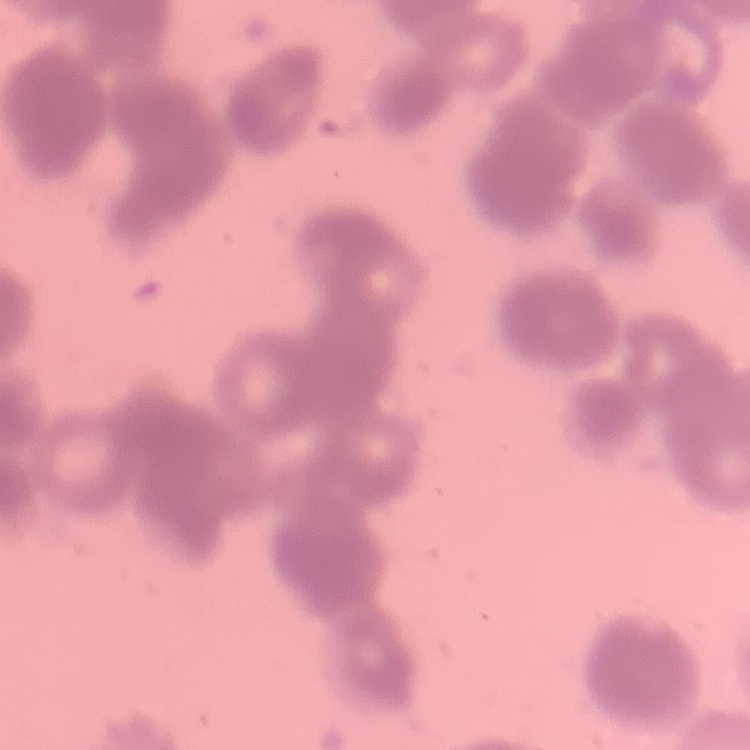
Summary:
  - Red blood cell morphology: rouleaux formation
  - Image type: square crop of a larger photomicrograph
  - Stain: Field's or Giemsa
  - Preparation: thin peripheral smear